Name the cell type shown.
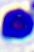
This is a leukocyte.

modality = photomicrograph
magnification = 400x